Assess this cell for malaria.
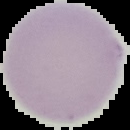
Uninfected.

Image is 130×130 pixels. The area outside the segmented cell region is set to black. From a thin blood smear.